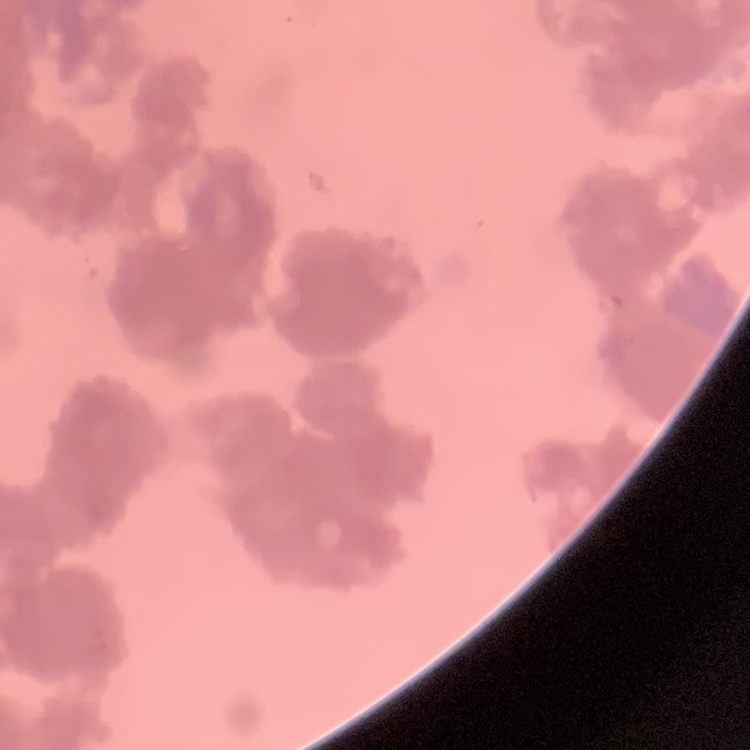

Summary:
  - Erythrocyte morphology: rouleaux formation
  - Image type: square crop of a larger photomicrograph
  - Stain: Field's or Giemsa
  - Preparation: thin peripheral smear